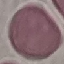
Summary:
  - Malaria status: uninfected
  - Capture: smartphone camera at the microscope eyepiece
  - Preparation: thin blood smear
  - Stain: Giemsa
  - Image type: automatically extracted cell patch, resized to 64 × 64 pixels